Classify this cell by malaria status.
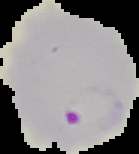

Parasitized.

Segmented cell region on a black background. Image is 139×154 pixels. From a thin blood film.